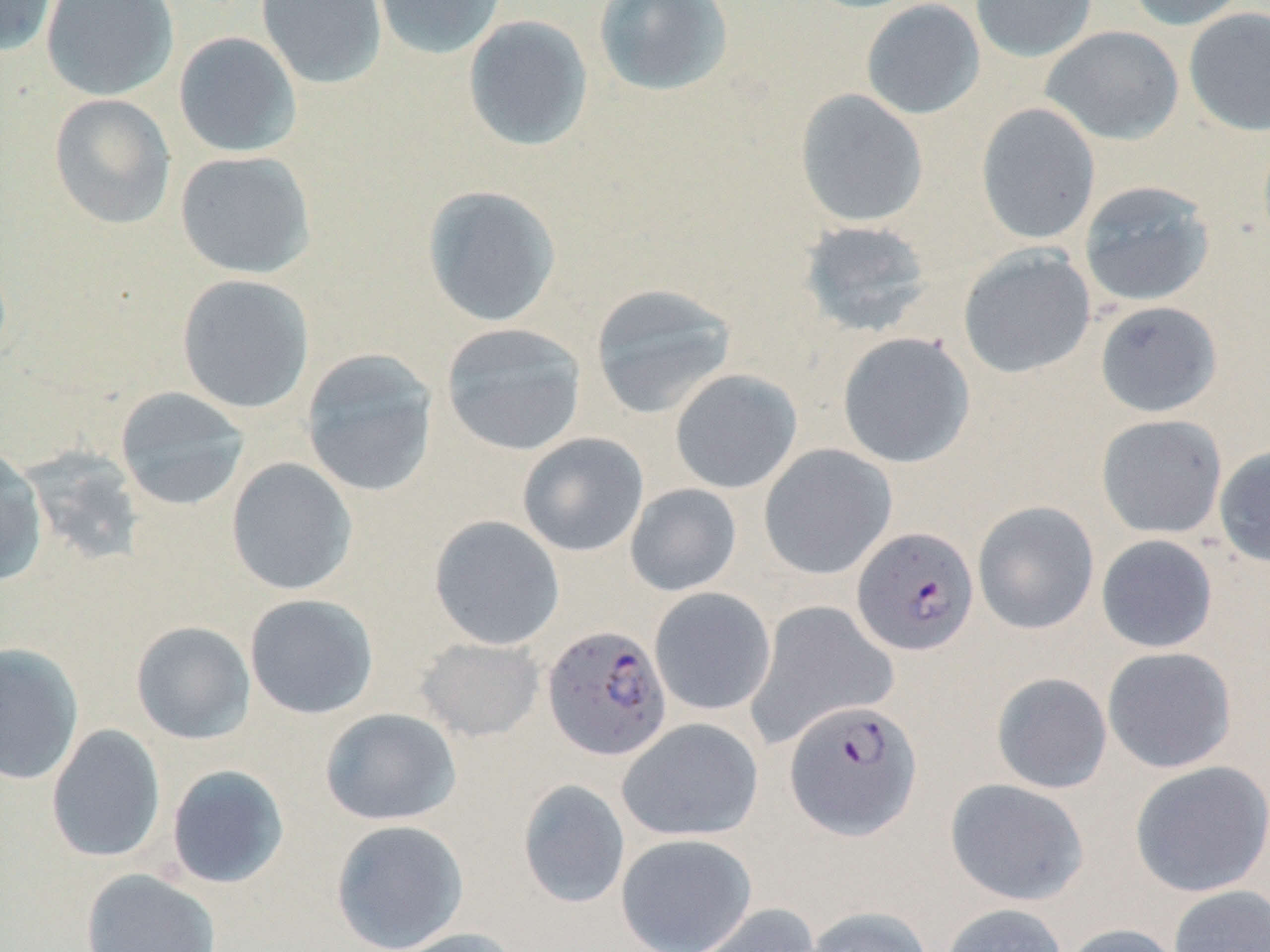
{
  "slide_level_diagnosis": "Plasmodium falciparum",
  "image_size": "1270×952 pixels",
  "field_of_view": "one of a larger specimen",
  "preparation": "thin blood film",
  "plasmodium_falciparum_infected_red_blood_cell_locations": "approximate bounding boxes as (x1,y1)-(x2,y2) corner pairs in pixels: (852,526)-(979,656), (541,624)-(672,761), (784,698)-(923,840)",
  "stain": "May-Grünwald-Giemsa",
  "uninfected_red_blood_cell_locations": "approximate bounding boxes as (x1,y1)-(x2,y2) corner pairs in pixels: (0,0)-(58,56), (40,0)-(179,102), (255,0)-(387,90), (372,0)-(507,60), (593,0)-(734,97), (861,0)-(985,120), (970,0)-(1098,62), (1125,0)-(1250,30), (1184,7)-(1270,136), (462,15)-(594,152), (1041,25)-(1185,145), (173,31)-(302,158), (794,89)-(928,228), (48,94)-(177,229), (975,103)-(1101,245), (174,150)-(317,279), (1078,180)-(1216,307), (421,185)-(562,328), (797,219)-(934,338), (958,245)-(1096,379), (176,274)-(315,414), (590,283)-(736,419), (1094,300)-(1223,418), (440,323)-(587,456), (837,331)-(976,469), (300,348)-(439,499), (669,368)-(803,494), (114,387)-(251,511), (1096,414)-(1228,539), (516,432)-(649,557), (758,444)-(897,580), (1213,445)-(1270,567), (18,446)-(146,567), (0,447)-(49,586), (226,457)-(358,596), (625,483)-(742,597), (972,501)-(1100,635), (429,515)-(565,651), (1096,534)-(1218,653), (649,587)-(776,716), (244,593)-(379,719), (745,600)-(900,749), (131,621)-(256,745), (415,636)-(545,742), (0,642)-(84,785), (1102,647)-(1237,773), (991,672)-(1112,794), (320,707)-(461,826), (616,717)-(763,842), (46,724)-(166,864), (1129,760)-(1270,897), (165,764)-(290,889), (944,778)-(1089,906), (518,779)-(630,909), (330,818)-(469,952), (615,833)-(758,952), (80,868)-(221,952), (1168,885)-(1270,952), (687,903)-(822,952), (939,903)-(1069,952), (802,905)-(934,952), (1061,923)-(1183,952), (391,927)-(525,952)",
  "magnification": "1000x",
  "modality": "optical microscopy"
}